Identify the parasite.
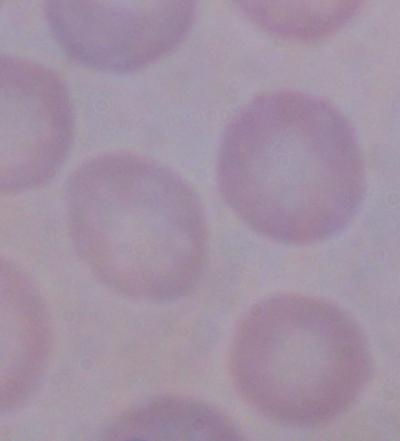

This is a trypanosome.

Captured at 1000x magnification. Micrograph.